Describe the morphology of the red blood cells.
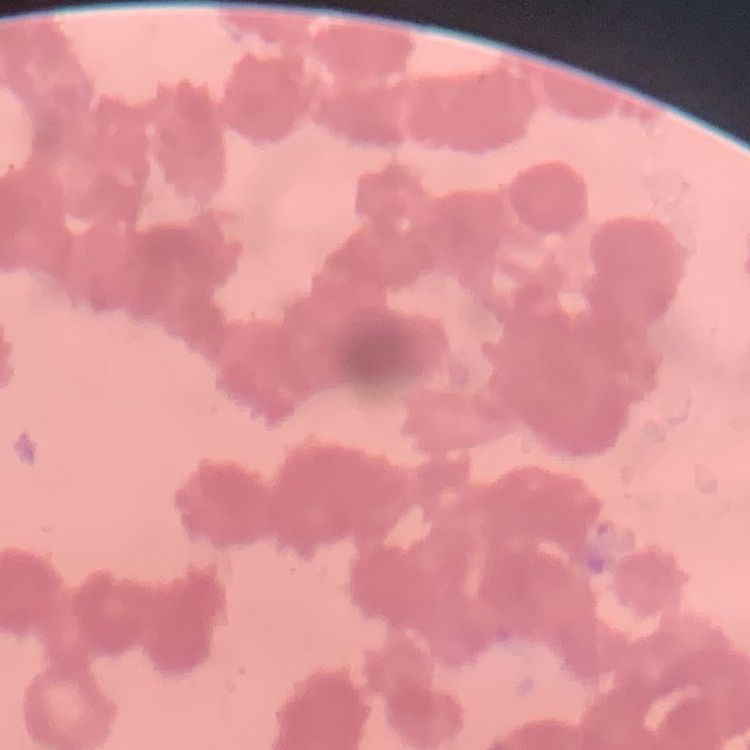
Rouleaux formation.

image type = square crop of a larger photomicrograph
preparation = thin peripheral smear
stain = Field's or Giemsa